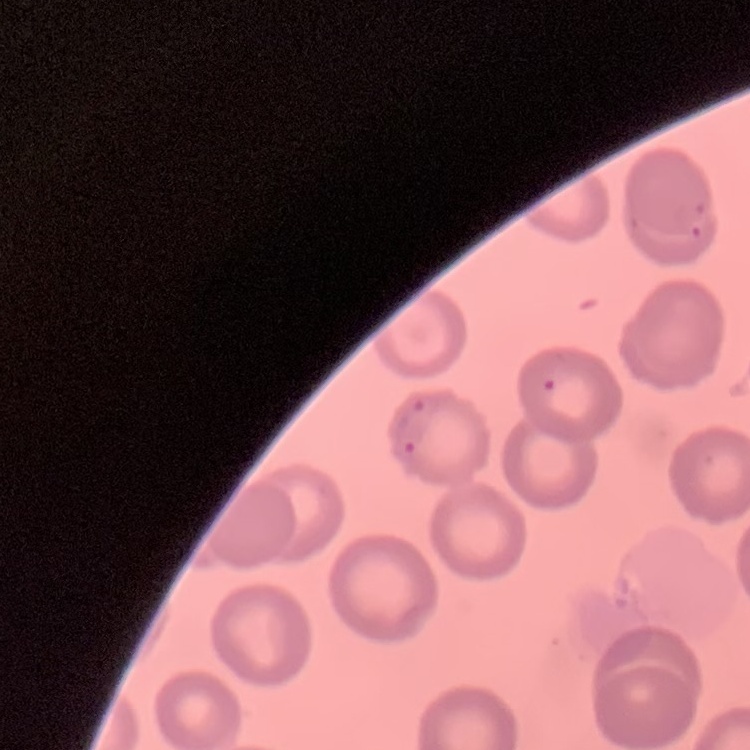 The red blood cells exhibit no rouleaux formation. One tile cut from a larger photomicrograph. Stained with either Field's or Giemsa. Thin peripheral smear.